Assess this cell for malaria.
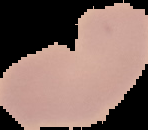

It is uninfected.

image_size: 148×130 pixels
image_type: cell region segmented out of the field of view; surrounding area masked to black
preparation: thin blood smear